Report the malaria status of this cell.
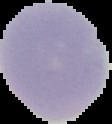
Uninfected.

Summary:
  - Image size: 112×124 pixels
  - Image type: segmented cell region with the area outside set to black
  - Preparation: thin blood smear